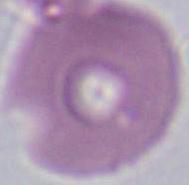 1000x magnification. A red blood cell is shown. Photomicrograph.